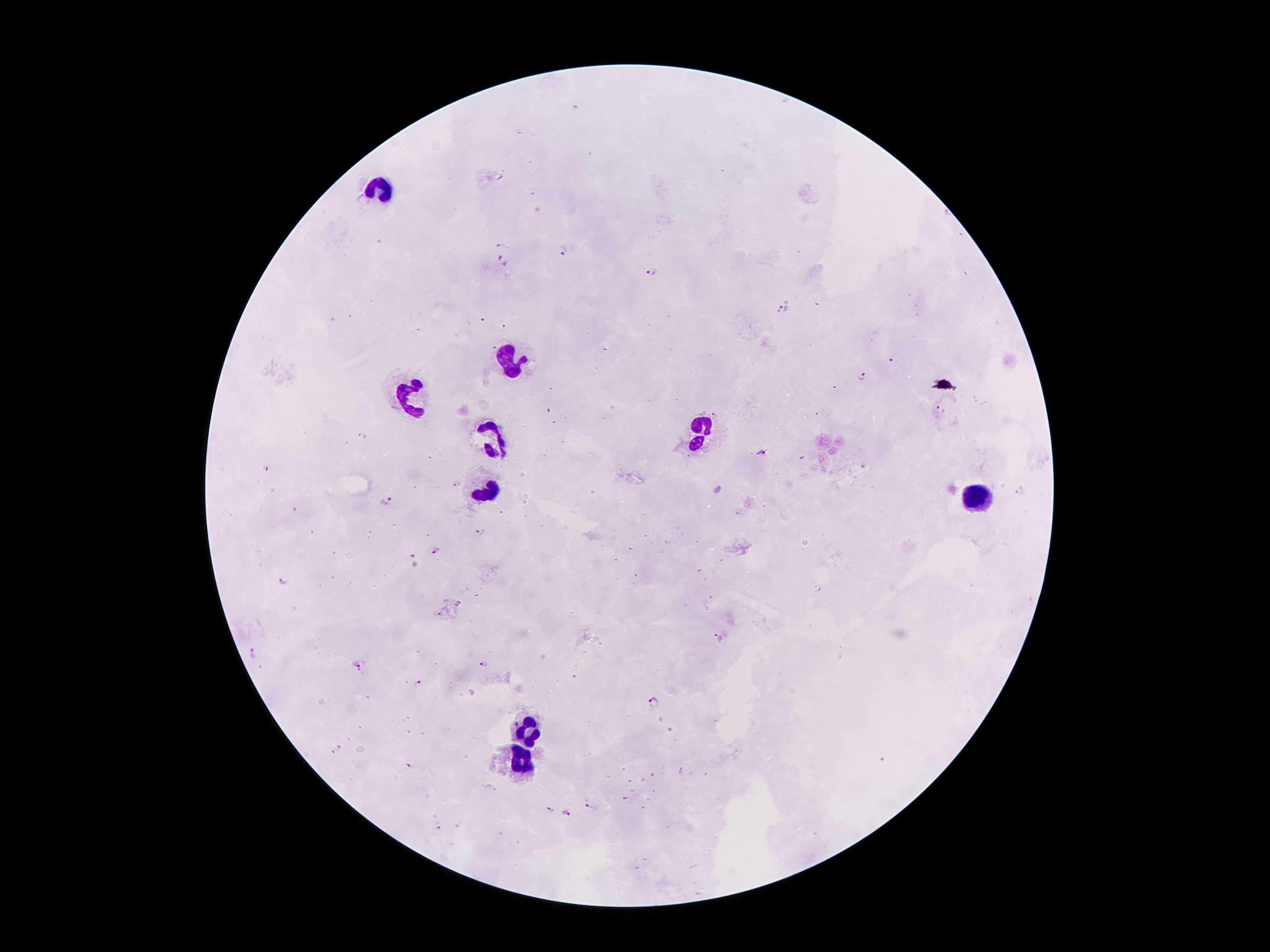
Approximate centers as {x, y} in pixels.
Summary:
  - Leukocyte locations: {379, 187}, {509, 362}, {413, 398}, {704, 427}, {490, 439}, {490, 493}, {972, 493}, {527, 730}, {520, 761}
  - Malaria parasite locations: {501, 244}, {562, 251}, {502, 261}, {650, 273}, {784, 307}, {894, 361}, {864, 377}, {941, 408}, {548, 411}, {717, 414}, {361, 435}, {762, 453}, {264, 468}, {455, 483}, {1021, 491}, {386, 500}, {481, 529}, {435, 550}, {415, 560}, {283, 581}, {819, 589}, {460, 603}, {437, 614}, {719, 636}, {250, 652}, {482, 661}, {357, 664}, {418, 683}, {653, 702}, {339, 747}, {332, 753}, {411, 766}, {589, 806}, {549, 811}, {566, 813}, {437, 829}
  - Preparation: thick blood smear
  - Image size: 1270×952 pixels
  - Field of view: single
  - Capture: smartphone camera through the microscope eyepiece
  - Magnification: 100x
  - Patient malaria status: positive for Plasmodium falciparum
  - Stain: Giemsa